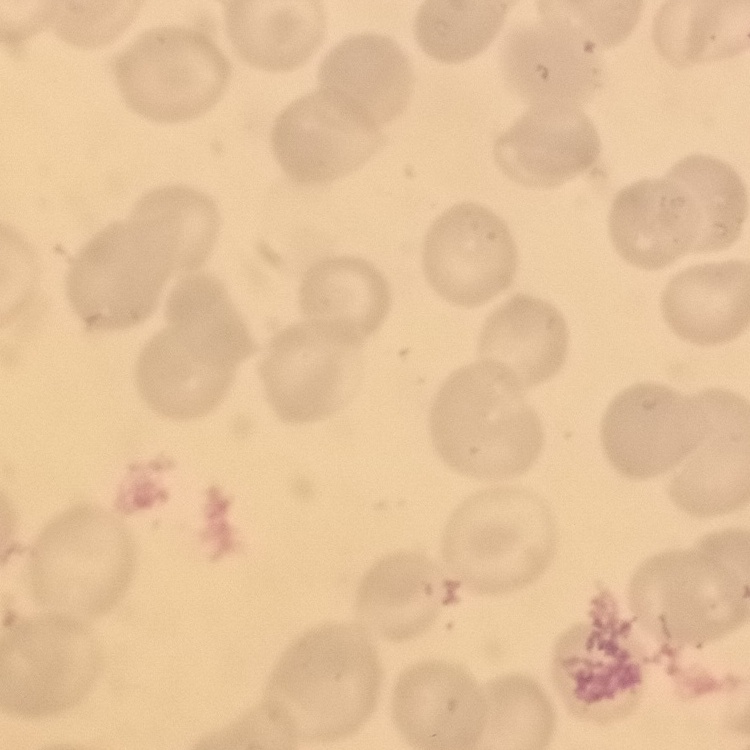

Summary:
  - Erythrocyte morphology: no rouleaux formation
  - Preparation: thin peripheral smear
  - Stain: Field's or Giemsa
  - Image type: square crop of a larger photomicrograph